Describe the morphology of the red blood cells.
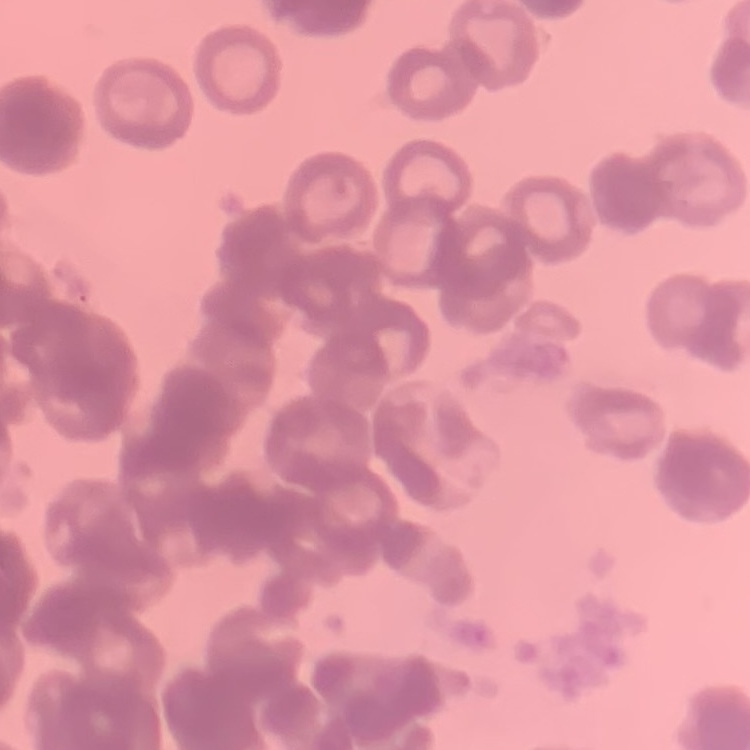

They show rouleaux formation.

Thin blood film. Field's or Giemsa stain. Square crop of a larger photomicrograph.